Look for Plasmodium parasites.
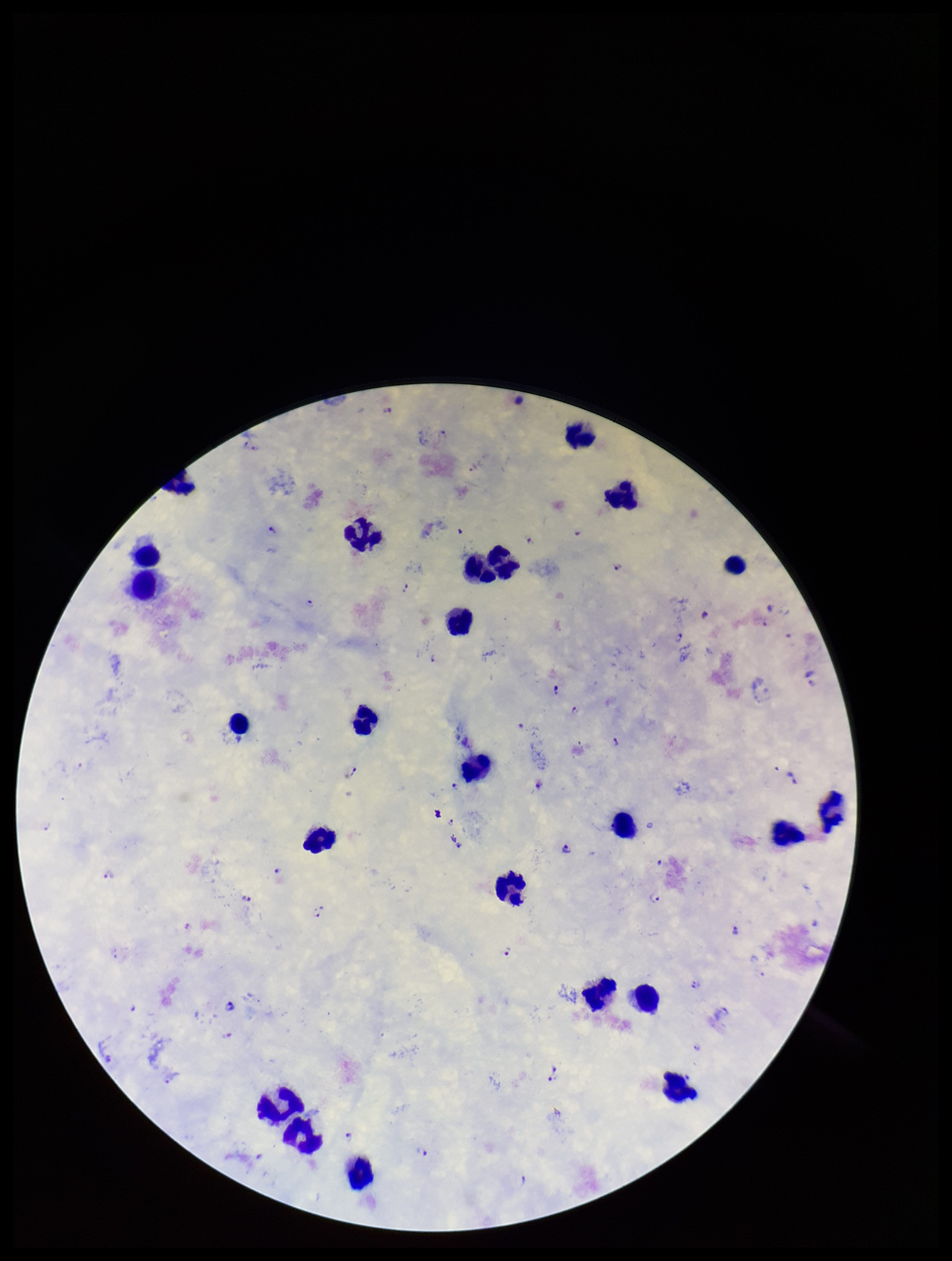

Seen.

Parasite count: 34. Preparation: thick blood smear. Image is 952×1261 pixels. Stained with Giemsa. Smartphone photograph taken through the eyepiece of a microscope. Patient malaria status: infected. One field from this slide. Leukocyte count: 24. Species reported for this patient: Plasmodium falciparum.